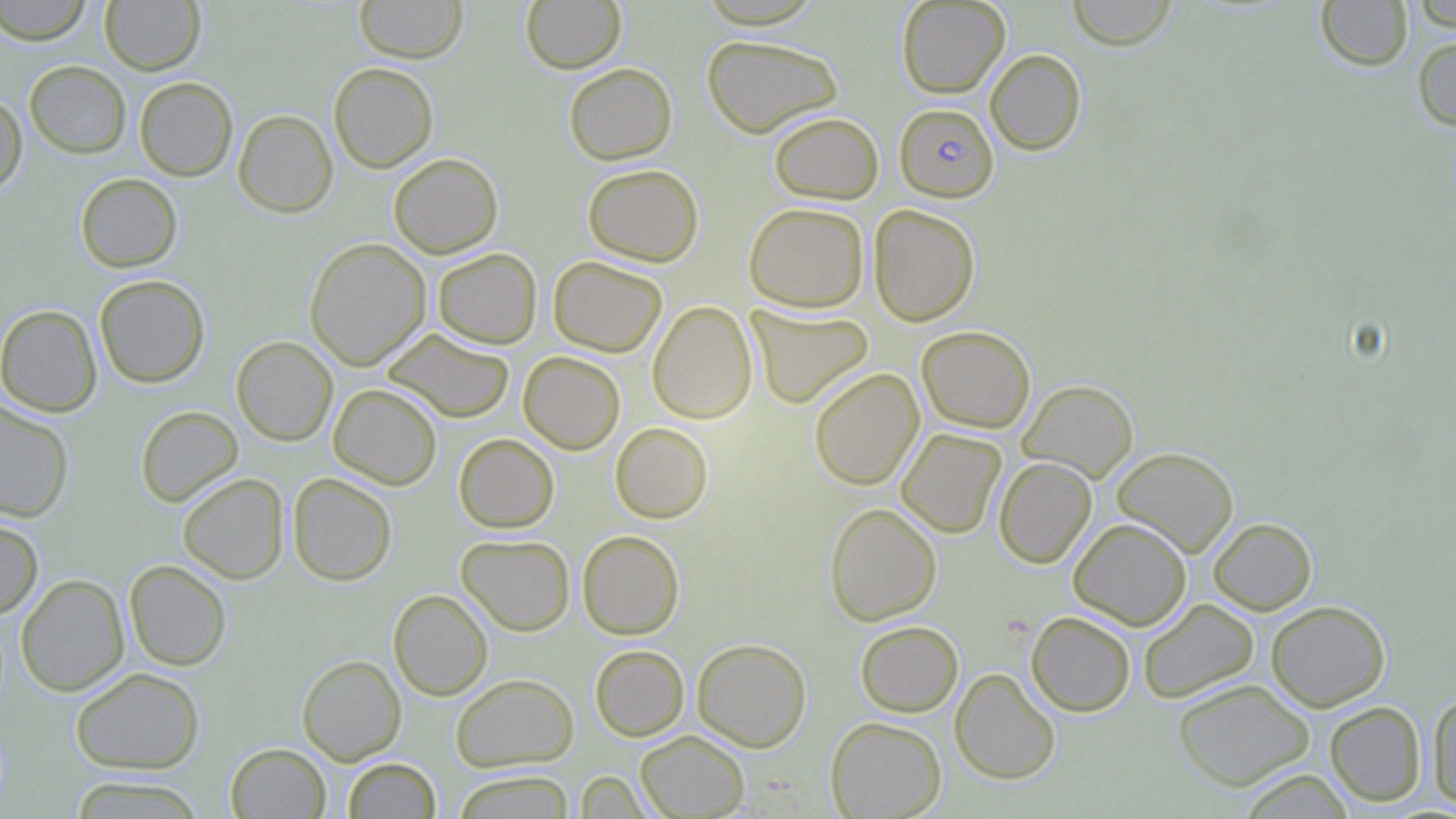
Summary:
  - Coordinate format: approximate bounding boxes as (x1, y1, x2, y2) in pixels
  - Plasmodium falciparum-infected red blood cell locations: (894, 103, 998, 202)
  - Uninfected red blood cell locations: (0, 0, 94, 45), (354, 0, 467, 63), (896, 0, 1010, 98), (1065, 0, 1181, 50), (1315, 0, 1413, 71), (1409, 0, 1456, 30), (100, 1, 205, 74), (521, 1, 626, 74), (701, 34, 842, 138), (1412, 34, 1456, 132), (985, 49, 1087, 155), (24, 61, 131, 158), (328, 62, 438, 173), (564, 62, 677, 165), (134, 76, 238, 181), (0, 92, 28, 195), (233, 109, 338, 217), (769, 111, 883, 204), (388, 153, 503, 258), (582, 164, 704, 267), (75, 172, 183, 272), (743, 202, 869, 312), (868, 204, 980, 327), (304, 238, 431, 370), (432, 248, 542, 349), (548, 256, 667, 357), (94, 274, 210, 388), (647, 300, 757, 423), (0, 305, 102, 417), (746, 305, 874, 409), (917, 325, 1035, 433), (384, 327, 514, 423), (231, 336, 338, 446), (518, 351, 625, 455), (809, 368, 924, 490), (1018, 379, 1138, 483), (328, 383, 443, 490), (0, 400, 74, 522), (134, 406, 243, 507), (610, 423, 713, 523), (896, 428, 1007, 538), (454, 433, 559, 533), (1111, 446, 1239, 557), (993, 457, 1096, 568), (177, 472, 289, 584), (287, 472, 397, 586), (824, 502, 942, 626), (0, 516, 44, 619), (1208, 517, 1317, 615), (1068, 518, 1191, 630), (577, 530, 684, 639), (456, 533, 575, 635), (124, 559, 232, 671), (16, 573, 130, 696), (388, 589, 493, 701), (1138, 598, 1259, 704), (1266, 600, 1390, 712), (1026, 611, 1136, 717), (855, 620, 963, 717), (691, 638, 812, 752), (589, 645, 689, 741), (297, 655, 406, 764), (70, 667, 205, 774), (950, 668, 1061, 785), (450, 673, 579, 771), (1172, 678, 1315, 790), (1427, 690, 1456, 811), (1324, 701, 1426, 807), (825, 716, 946, 818), (636, 730, 749, 818), (225, 743, 330, 818), (342, 758, 440, 818), (1237, 768, 1355, 818), (451, 770, 576, 818), (574, 770, 654, 818), (68, 775, 207, 818)
  - Slide-level diagnosis: Plasmodium falciparum
  - Stain: May-Grünwald-Giemsa
  - Preparation: thin blood smear
  - Field of view: single
  - Image size: 1456×819 pixels
  - Magnification: 1000x
  - Modality: optical microscopy